Classify this cell by malaria status.
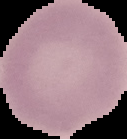
It is uninfected.

Summary:
  - Preparation: thin blood film
  - Image type: segmented cell region with the area outside set to black
  - Image size: 127×139 pixels